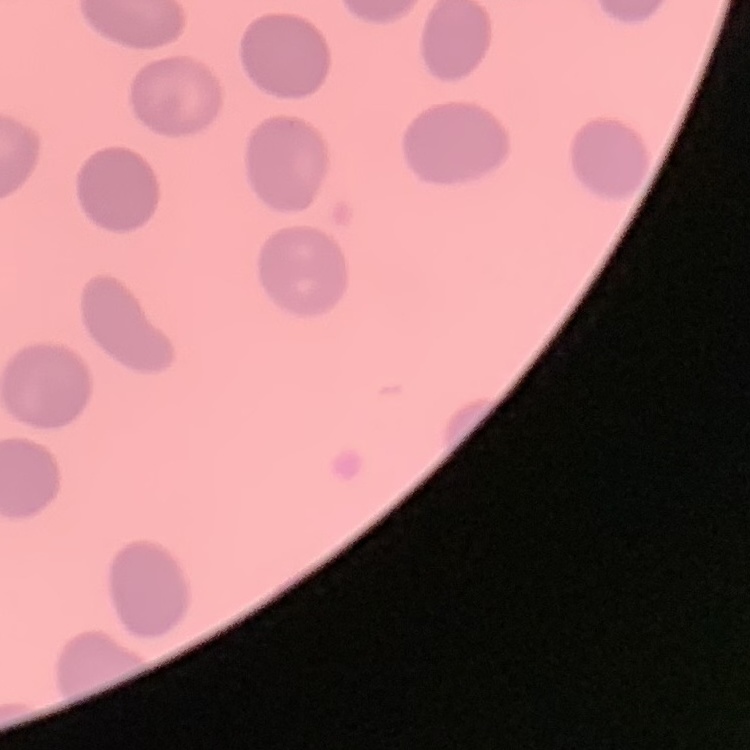
The red blood cells show no rouleaux formation. Thin blood smear. Field's or Giemsa stain. Square crop of a larger photomicrograph.